Point out Plasmodium parasites and leukocytes.
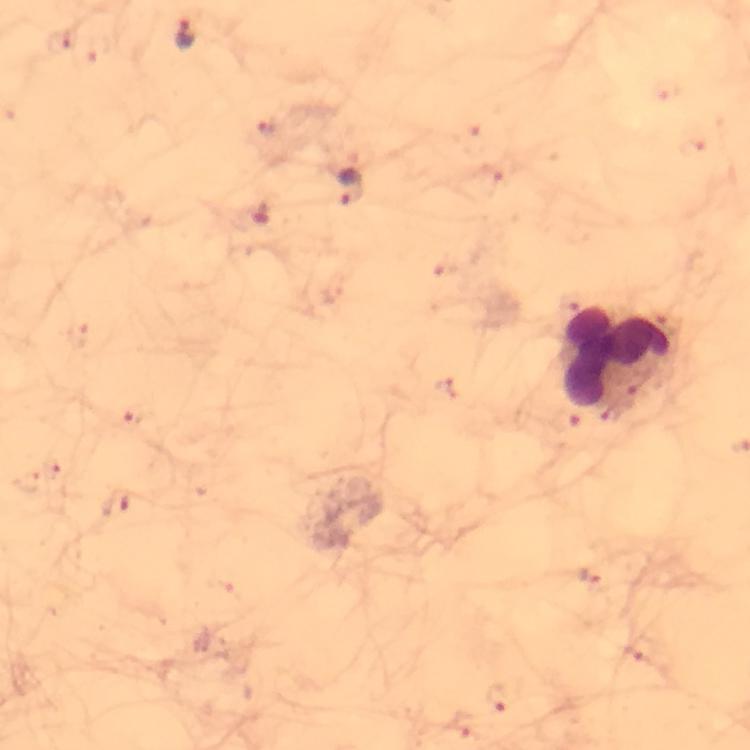

Approximate object centers, in pixels from the top-left corner.
Plasmodium parasites: (x=187, y=34), (x=355, y=190), (x=261, y=213), (x=137, y=416), (x=116, y=504), (x=586, y=577).
Leukocytes: (x=618, y=358).

Photographed through the microscope with a smartphone camera. Immersion oil was used. Thick smear. Giemsa-stained preparation. At 100x magnification. Cropped region of a single field of view. From a diagnostic examination for malaria. Image is 750×750 pixels.